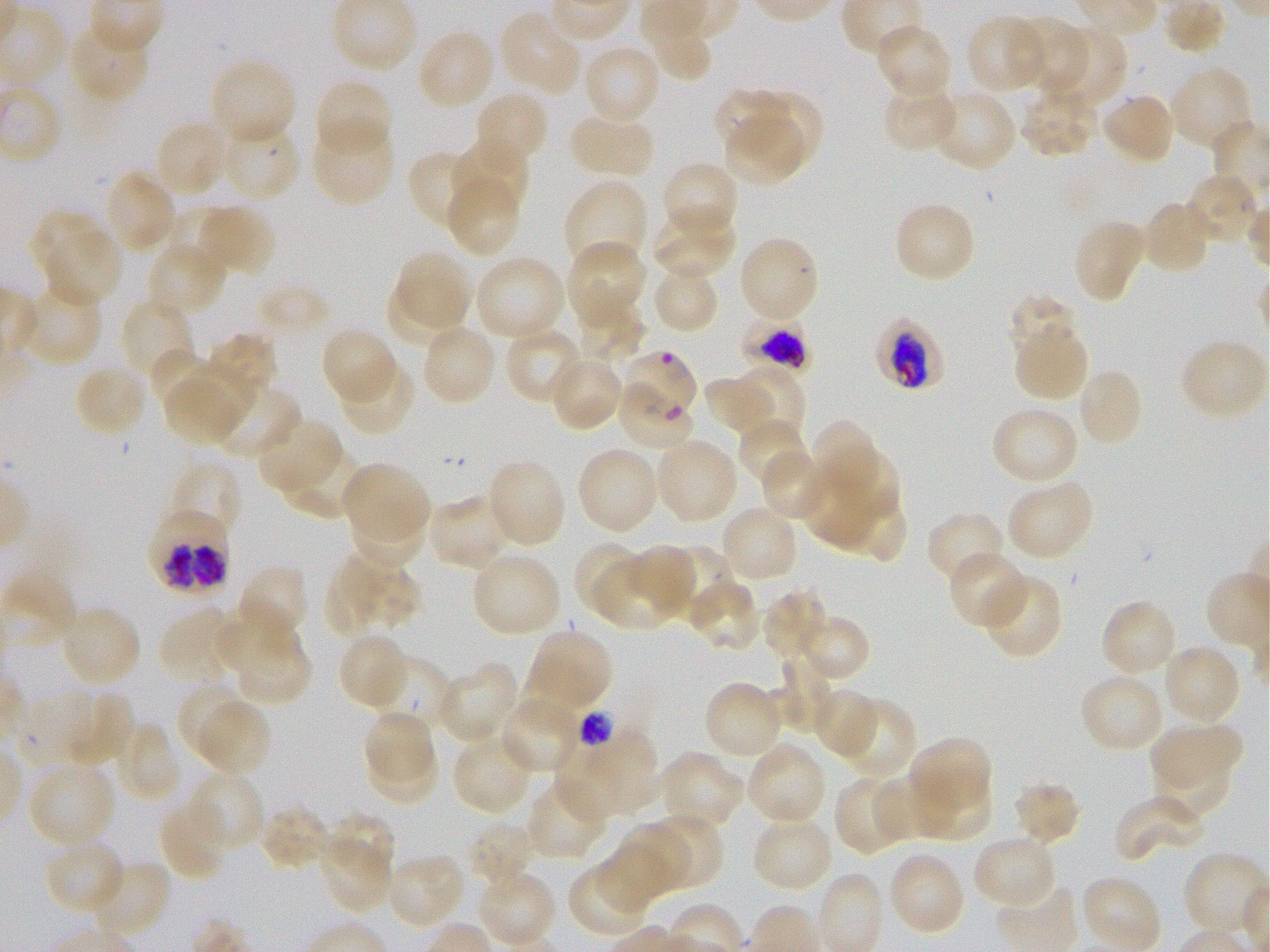
Approximate bounding boxes as {x1, y1, x2, y2} in pixels. Not every red blood cell is marked. A life-cycle stage — or a range of stages, where the recorded stages span more than one — follows each staged infected red blood cell.
Summary:
  - Locations of uninfected red blood cells: {1162, 0, 1225, 54}, {498, 10, 583, 97}, {965, 15, 1049, 94}, {640, 16, 713, 81}, {70, 19, 151, 105}, {1008, 19, 1086, 89}, {873, 23, 954, 100}, {1043, 25, 1127, 111}, {416, 27, 498, 111}, {582, 43, 662, 126}, {208, 57, 296, 147}, {1169, 66, 1254, 152}, {313, 78, 391, 160}, {881, 81, 959, 154}, {714, 88, 789, 152}, {930, 88, 1018, 172}, {1017, 88, 1099, 159}, {473, 89, 550, 169}, {1100, 91, 1177, 166}, {752, 93, 825, 163}, {568, 110, 655, 181}, {723, 112, 808, 181}, {153, 119, 231, 199}, {310, 120, 395, 206}, {219, 123, 302, 202}, {449, 139, 529, 218}, {405, 149, 482, 233}, {660, 161, 740, 239}, {103, 170, 178, 255}, {445, 172, 522, 258}, {1184, 172, 1263, 247}, {563, 176, 649, 275}, {173, 200, 245, 272}, {893, 200, 976, 284}, {1140, 200, 1212, 277}, {203, 205, 275, 278}, {648, 206, 737, 281}, {30, 210, 103, 277}, {1071, 218, 1148, 302}, {44, 234, 121, 309}, {737, 235, 821, 324}, {147, 240, 230, 317}, {566, 240, 647, 330}, {395, 251, 473, 328}, {473, 255, 566, 343}, {650, 262, 719, 335}, {572, 279, 644, 367}, {388, 281, 465, 348}, {18, 283, 102, 367}, {1006, 295, 1077, 359}, {119, 298, 194, 383}, {419, 323, 498, 407}, {319, 326, 399, 406}, {504, 326, 585, 405}, {1014, 328, 1088, 403}, {208, 335, 275, 395}, {1179, 338, 1269, 422}, {148, 348, 215, 417}, {548, 354, 625, 431}, {336, 359, 417, 437}, {73, 362, 150, 437}, {184, 362, 256, 425}, {737, 365, 805, 439}, {1075, 367, 1145, 448}, {703, 378, 774, 437}, {204, 382, 299, 459}, {167, 386, 240, 445}, {990, 405, 1080, 487}, {255, 417, 343, 497}, {736, 417, 810, 489}, {813, 422, 870, 489}, {653, 436, 739, 526}, {281, 444, 366, 521}, {823, 445, 904, 521}, {575, 446, 660, 536}, {760, 449, 830, 524}, {169, 458, 244, 541}, {486, 458, 567, 549}, {342, 461, 430, 543}, {807, 466, 873, 549}, {1004, 478, 1095, 562}, {426, 494, 514, 571}, {351, 497, 429, 572}, {851, 501, 908, 564}, {719, 504, 800, 585}, {926, 510, 1006, 586}, {574, 541, 648, 616}, {625, 544, 698, 615}, {659, 548, 732, 625}, {471, 549, 563, 639}, {592, 550, 689, 631}, {946, 550, 1031, 630}, {324, 553, 422, 638}, {237, 564, 309, 644}, {980, 573, 1064, 660}, {687, 577, 761, 654}, {763, 589, 831, 663}, {1099, 598, 1180, 679}, {215, 600, 301, 676}, {59, 604, 141, 689}, {158, 607, 243, 688}, {792, 613, 870, 682}, {227, 625, 313, 707}, {525, 628, 613, 715}, {335, 632, 409, 711}, {1161, 643, 1242, 727}, {766, 650, 831, 735}, {370, 656, 456, 734}, {435, 661, 520, 744}, {1078, 671, 1165, 755}, {703, 680, 780, 756}, {809, 686, 880, 759}, {180, 687, 244, 757}, {71, 692, 133, 770}, {498, 692, 583, 774}, {834, 698, 915, 782}, {200, 702, 271, 777}, {362, 709, 434, 781}, {115, 721, 181, 803}, {1149, 722, 1244, 797}, {556, 728, 660, 820}, {451, 732, 538, 815}, {906, 737, 992, 821}, {745, 739, 827, 827}, {367, 740, 440, 800}, {1148, 749, 1234, 825}, {659, 750, 746, 832}, {26, 760, 117, 851}, {915, 767, 991, 839}, {186, 771, 266, 853}, {834, 773, 913, 854}, {872, 774, 957, 839}, {526, 779, 608, 861}, {1011, 780, 1082, 846}, {1114, 793, 1208, 863}, {159, 796, 231, 881}, {260, 804, 335, 870}, {327, 811, 397, 879}, {657, 813, 725, 886}, {750, 816, 834, 892}, {618, 820, 692, 895}, {467, 821, 539, 888}, {971, 833, 1058, 910}, {319, 838, 388, 914}, {43, 839, 126, 914}, {598, 846, 668, 911}, {887, 850, 967, 937}, {385, 852, 466, 927}, {1182, 853, 1268, 939}, {85, 859, 171, 940}, {565, 867, 645, 939}, {476, 870, 556, 948}, {1080, 875, 1162, 952}
  - Locations of infected red blood cells: {742, 310, 812, 379} early trophozoite to late schizont; {879, 322, 943, 389} early trophozoite to late schizont; {147, 507, 232, 594}
  - Locations of red blood cells of indeterminate infection status: {615, 350, 699, 423}, {614, 382, 696, 451}, {579, 709, 617, 743}
  - Donor blood group: O+
  - Field of view: one from this slide
  - Preparation: thin blood film
  - Culture: in-vitro P. falciparum strain 3D7, static
  - Image size: 1270×952 pixels
  - Objective: 100x, oil immersion, numerical aperture 1.25
  - Stain: Giemsa